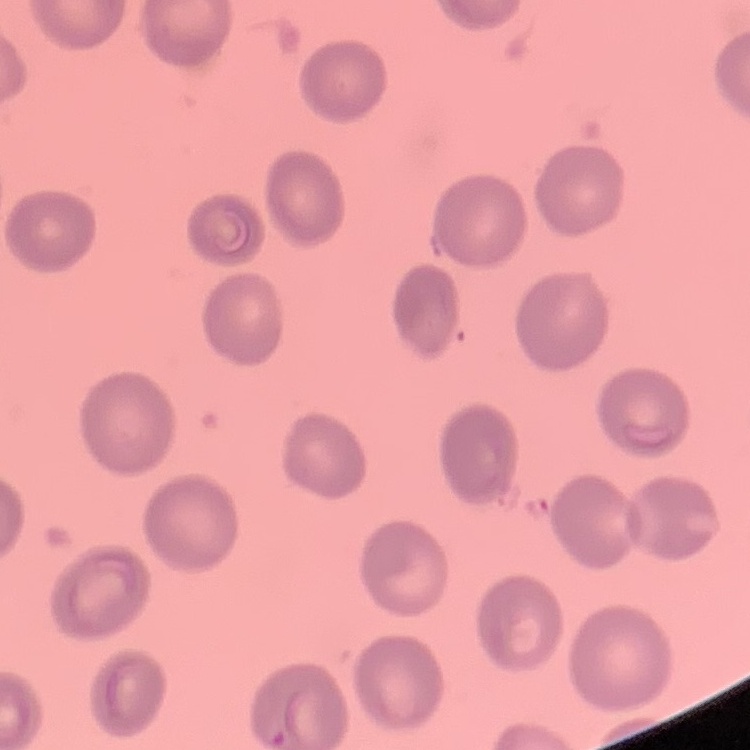

Summary:
  - Erythrocyte morphology: no rouleaux formation
  - Image type: square crop of a larger photomicrograph
  - Stain: Field's or Giemsa
  - Preparation: thin blood smear